Locate every Plasmodium vivax-infected red blood cell.
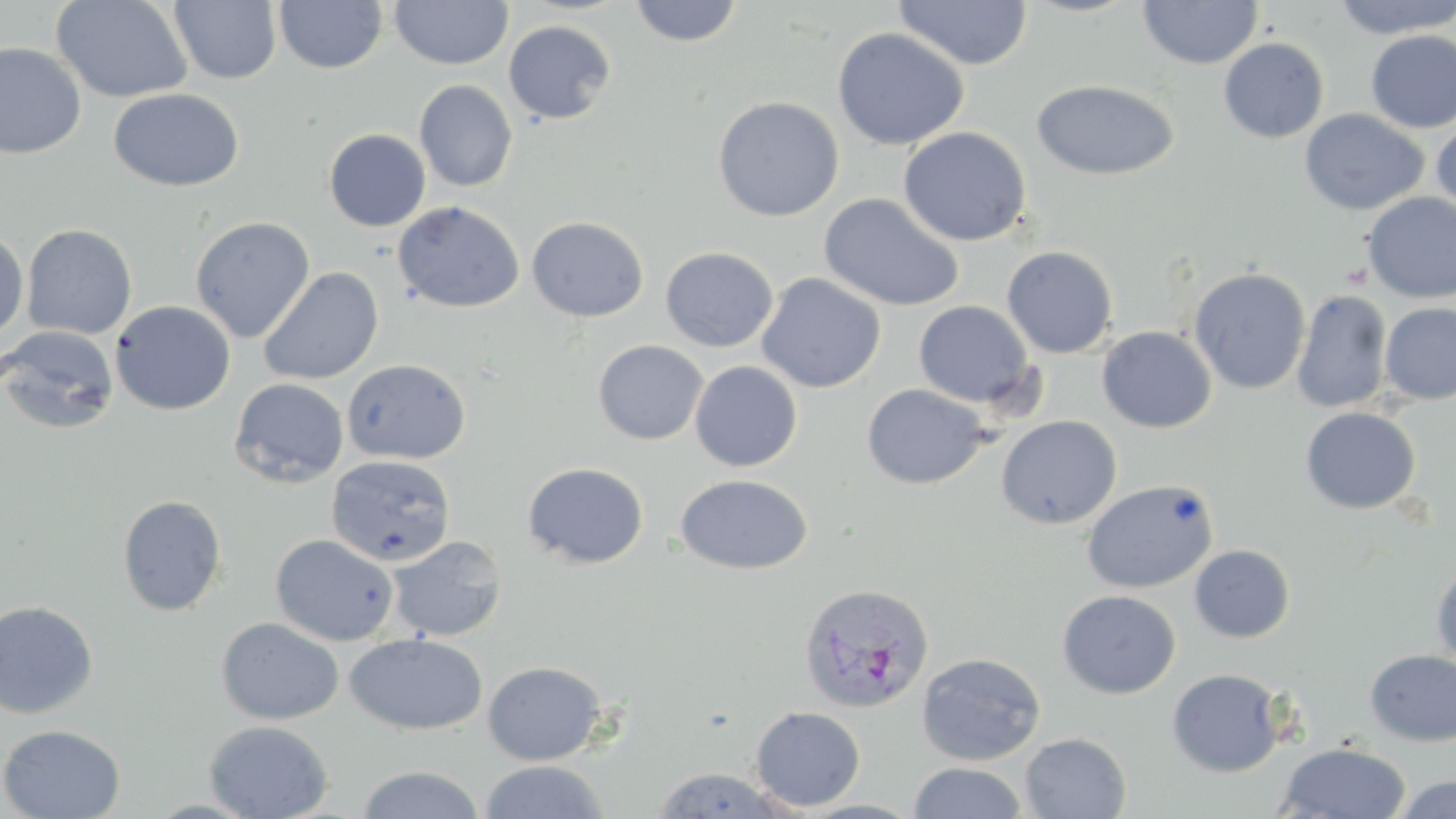
Approximate bounding boxes as (x1, y1, x2, y2) in pixels.
Plasmodium vivax-infected red blood cells: (799, 582, 934, 712).

{
  "slide_level_diagnosis": "Plasmodium vivax",
  "image_size": "1456×819 pixels",
  "magnification": "1000x",
  "preparation": "thin blood smear",
  "uninfected_red_blood_cell_locations": "approximate bounding boxes as (x1, y1, x2, y2) in pixels: (50, 0, 193, 104), (169, 0, 281, 85), (390, 0, 513, 70), (628, 0, 745, 47), (1138, 0, 1262, 69), (1331, 0, 1456, 39), (274, 1, 388, 74), (893, 1, 1033, 70), (502, 20, 617, 125), (832, 27, 969, 151), (1365, 30, 1456, 134), (1218, 37, 1329, 143), (0, 42, 86, 159), (1031, 79, 1180, 181), (414, 80, 518, 192), (109, 88, 245, 192), (712, 95, 845, 221), (1299, 108, 1429, 216), (1431, 116, 1456, 223), (898, 126, 1032, 247), (323, 129, 431, 232), (818, 192, 965, 312), (1361, 192, 1456, 303), (392, 200, 524, 313), (190, 216, 315, 342), (527, 216, 648, 322), (21, 224, 137, 340), (0, 228, 29, 340), (1002, 245, 1119, 358), (660, 246, 778, 352), (259, 267, 384, 385), (1189, 267, 1311, 395), (756, 272, 886, 393), (1291, 289, 1393, 412), (110, 300, 236, 415), (914, 300, 1034, 406), (1379, 302, 1456, 405), (0, 325, 119, 435), (1097, 326, 1217, 434), (593, 340, 708, 445), (342, 359, 471, 465), (689, 361, 802, 472), (229, 378, 349, 488), (861, 384, 990, 489), (1299, 406, 1421, 514), (995, 415, 1122, 529), (326, 454, 456, 567), (522, 462, 649, 569), (675, 473, 813, 574), (1081, 478, 1219, 594), (116, 494, 227, 616), (270, 533, 399, 646), (386, 535, 507, 642), (1189, 544, 1296, 643), (1431, 562, 1456, 671), (1057, 589, 1180, 699), (0, 600, 99, 719), (215, 617, 344, 725), (345, 633, 488, 735), (1364, 649, 1456, 746), (916, 651, 1046, 765), (482, 660, 608, 766), (1166, 668, 1286, 778), (749, 706, 866, 811), (203, 719, 334, 819), (0, 724, 126, 818), (1020, 732, 1132, 819), (1276, 742, 1411, 818), (477, 759, 611, 819), (908, 762, 1029, 819), (355, 764, 487, 819), (647, 767, 800, 817), (1388, 775, 1456, 818)",
  "modality": "optical microscopy",
  "stain": "May-Grünwald-Giemsa",
  "field_of_view": "one of a larger specimen"
}